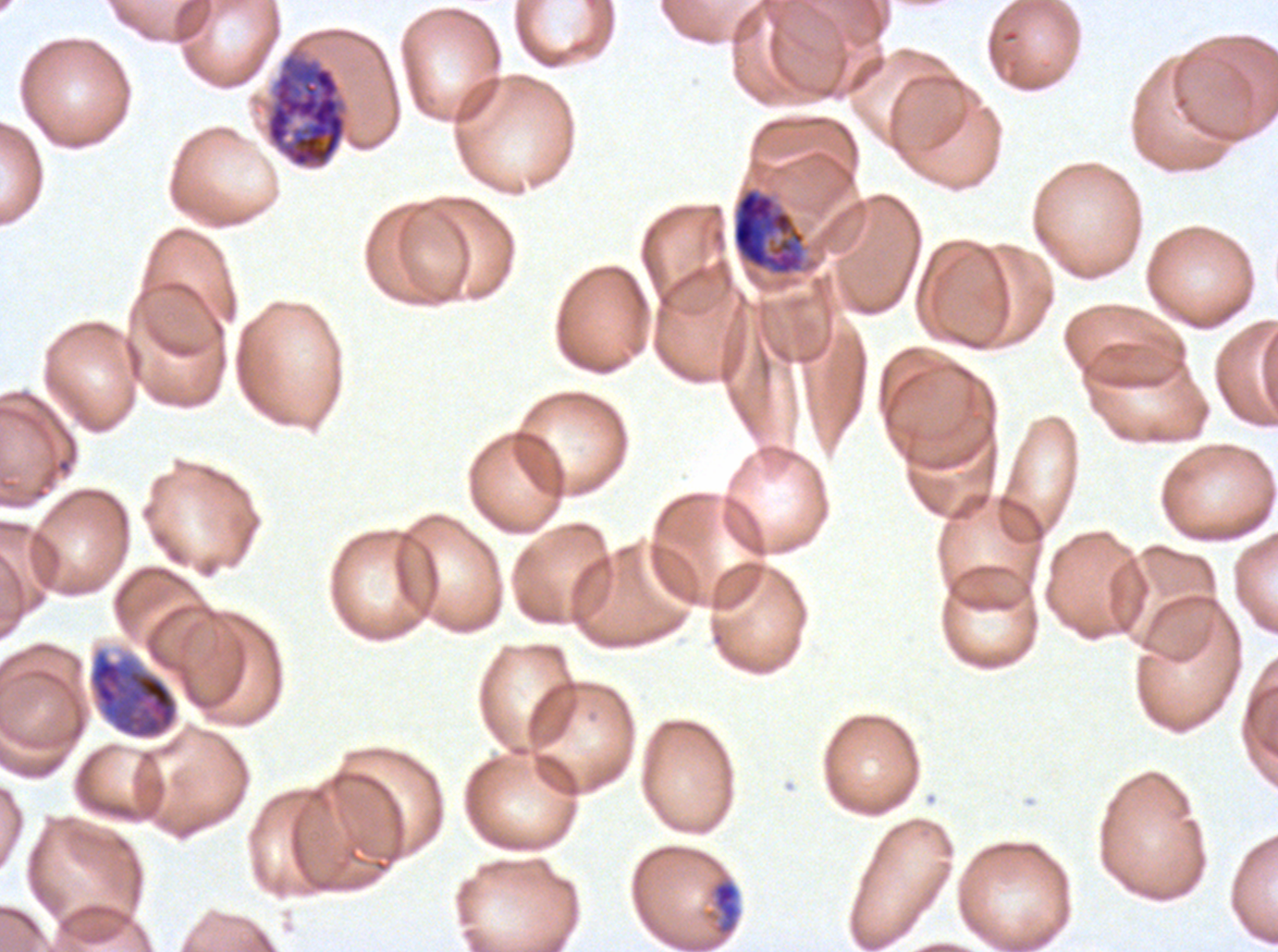
Approximate bounding rectangles given as corner coordinates in pixels from the top-left.
Summary:
  - Late-ring/early-trophozoite locations: (x1=705, y1=876, x2=743, y2=938)
  - Late schizont locations: (x1=265, y1=53, x2=347, y2=168)
  - Early schizont locations: (x1=731, y1=188, x2=805, y2=275), (x1=86, y1=643, x2=180, y2=742)
  - Image size: 1278×952 pixels
  - Preparation: thin blood film
  - Field of view: sub-image separated from a larger composite
  - Life-cycle stages observed: late-ring/early-trophozoite, early schizont, late schizont
  - Specimen: P. falciparum from a patient in The Gambia, cultured ex vivo for 24 to 48 hours
  - Stain: Giemsa